Comment on the morphology of the red blood cells.
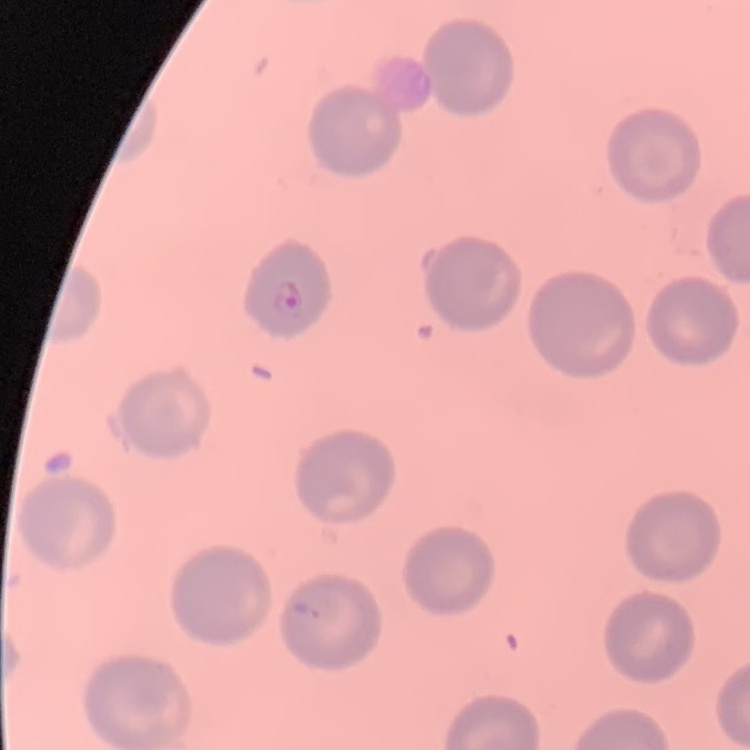

They show no rouleaux formation.

Square crop of a larger photomicrograph. Thin peripheral smear. Field's or Giemsa stain.